Identify the parasite.
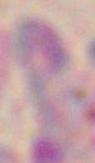
Toxoplasma gondii.

modality = photomicrograph
magnification = 1000x